Locate every leukocyte (white blood cell).
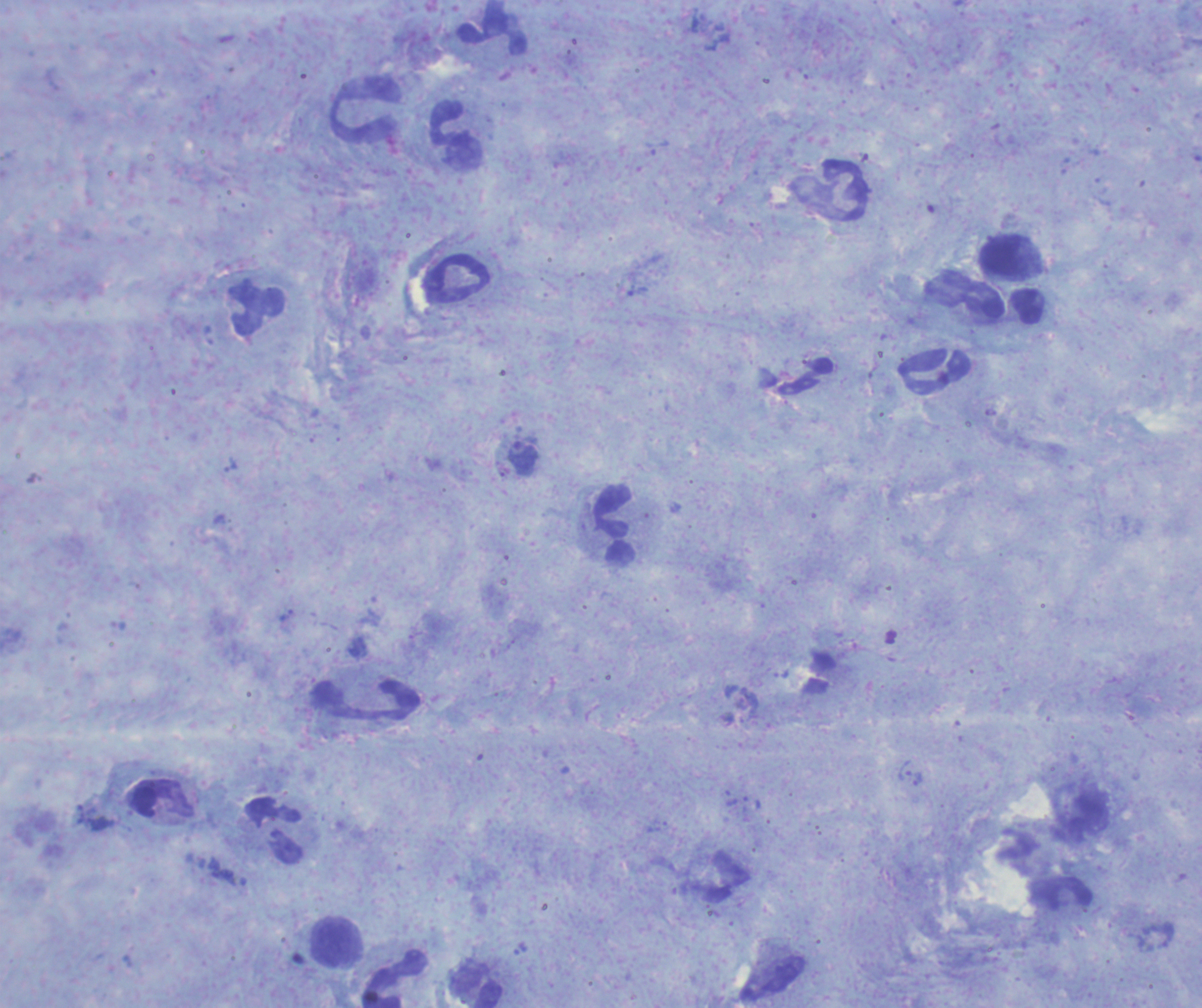
Approximate centers as {x, y} in pixels.
Leukocytes: {492, 34}, {365, 111}, {450, 124}, {829, 191}, {1002, 260}, {457, 278}, {257, 308}, {1028, 308}, {935, 373}, {614, 524}, {366, 699}, {162, 799}, {274, 833}, {1068, 894}, {333, 942}, {394, 979}, {477, 989}.

Approximate centers as {x, y} in pixels. Trophozoite locations: {523, 458}, {905, 770}, {917, 779}. Image is 1202×1008 pixels. 100x magnification. Background quality: satisfactory. One field from this slide. Thick blood smear. Previously used in a real diagnosis. Result: positive for malaria parasites. Coloration quality: good. Romanowsky stain.